Report the malaria status of this cell.
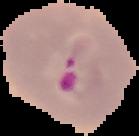

It is parasitized.

From a thin blood film. Segmented cell region on a black background. Image is 139×136 pixels.